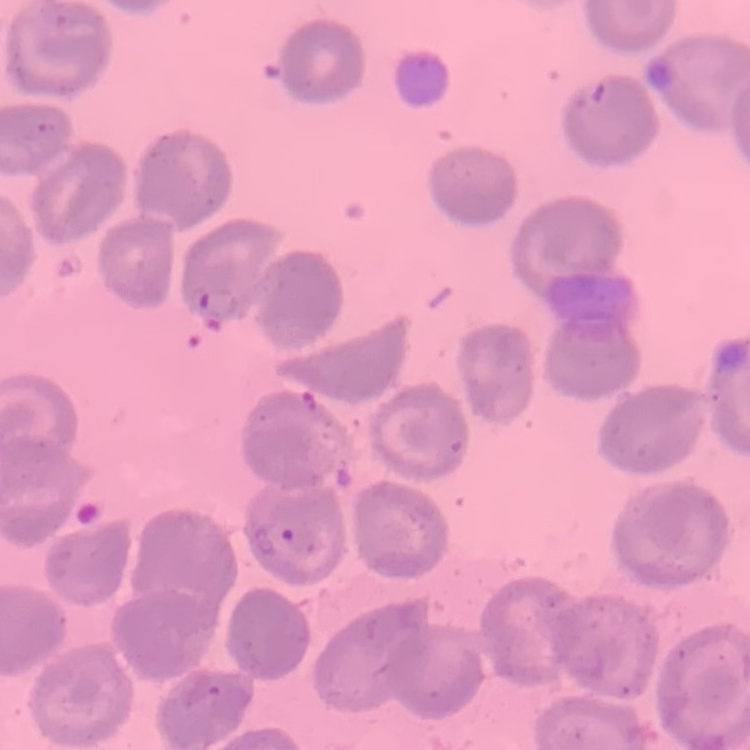
{
  "red_blood_cell_morphology": "no rouleaux formation",
  "stain": "Field's or Giemsa",
  "image_type": "square crop of a larger photomicrograph",
  "preparation": "thin peripheral smear"
}